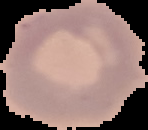
Summary:
  - Image size: 148×130 pixels
  - Image type: segmented cell region on a black background
  - Preparation: thin blood smear
  - Malaria status: uninfected